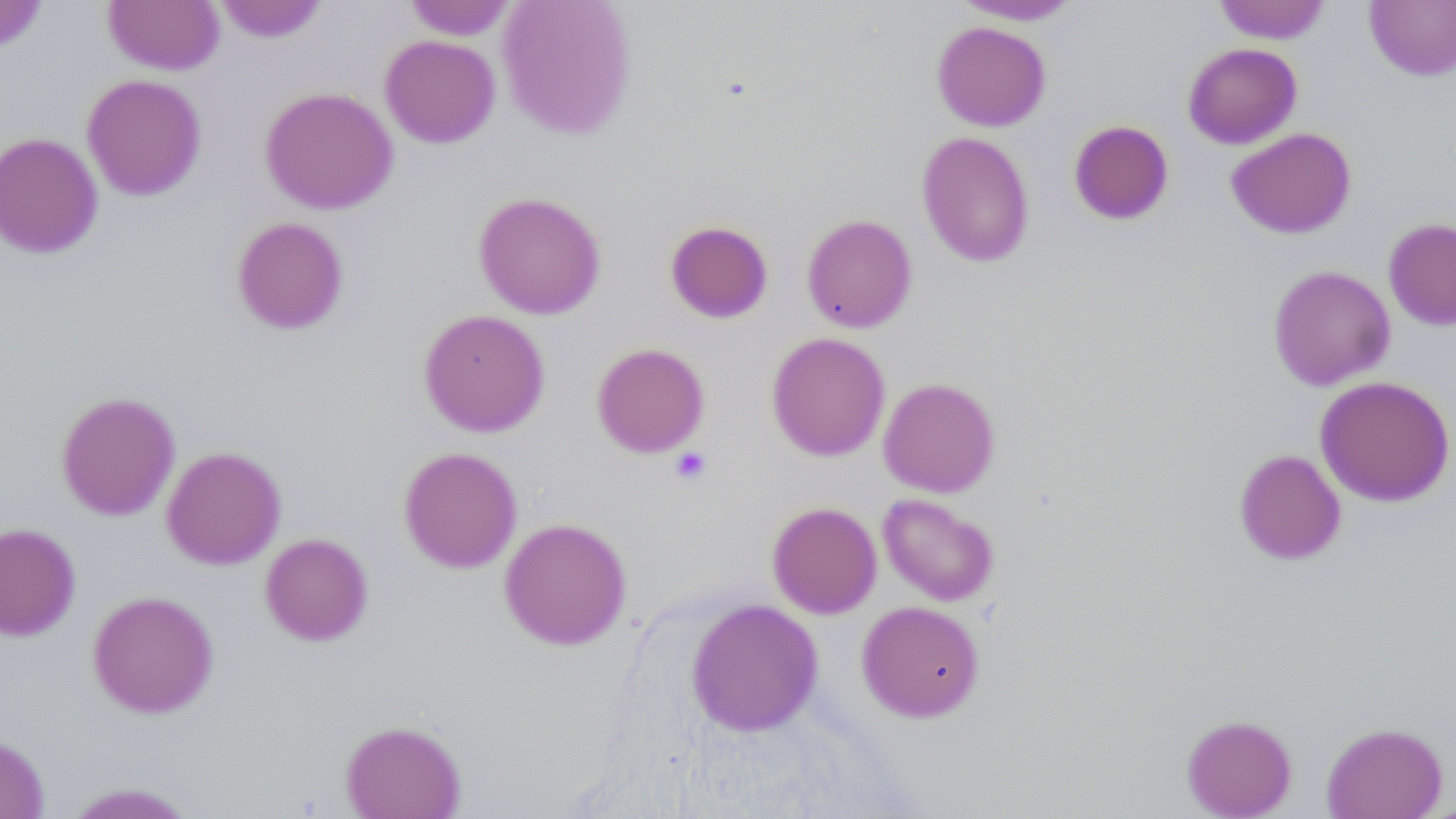

Approximate bounding boxes as (x1, y1, x2, y2) in pixels. Uninfected red blood cell locations: (214, 0, 328, 43), (404, 0, 516, 40), (497, 0, 638, 139), (951, 0, 1083, 25), (1213, 0, 1330, 44), (0, 1, 49, 53), (103, 1, 224, 75), (1364, 1, 1456, 81), (931, 21, 1051, 131), (379, 35, 501, 149), (1182, 42, 1302, 149), (82, 74, 207, 202), (259, 86, 398, 215), (1068, 119, 1175, 226), (1226, 128, 1356, 239), (916, 131, 1035, 268), (0, 132, 103, 259), (472, 191, 607, 319), (801, 213, 918, 333), (231, 216, 349, 335), (1383, 218, 1456, 330), (664, 220, 774, 324), (1267, 264, 1396, 391), (418, 309, 550, 437), (766, 332, 890, 461), (591, 342, 710, 458), (1315, 375, 1455, 507), (878, 377, 1000, 497), (55, 391, 181, 521), (161, 445, 287, 570), (398, 446, 523, 573), (1233, 449, 1346, 566), (877, 493, 1000, 606), (767, 501, 882, 618), (498, 517, 632, 651), (0, 522, 81, 641), (260, 533, 374, 646), (87, 590, 219, 718), (686, 598, 823, 737), (857, 600, 985, 722), (1181, 714, 1297, 818), (340, 720, 466, 818), (1321, 722, 1447, 819), (0, 733, 50, 819), (60, 782, 199, 818). Platelet locations: (669, 447, 712, 486). Slide-level diagnosis: no evidence of blood parasites. May-Grünwald-Giemsa-stained preparation. One field of a larger specimen. 1000x magnification. Thin blood smear. Image is 1456×819 pixels. Optical microscopy.